Locate every blood parasite and identify its species.
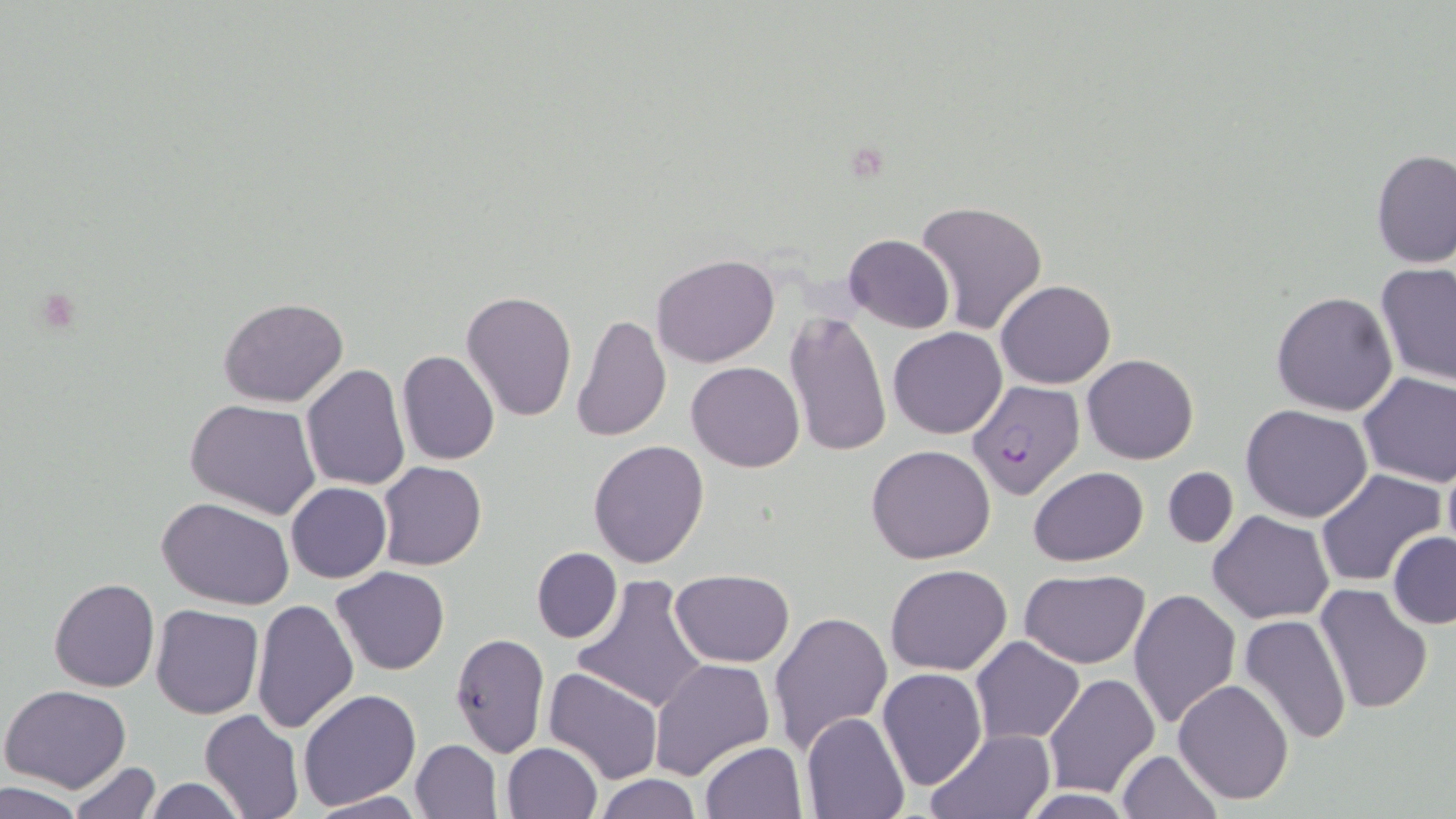
Approximate bounding boxes as (x1, y1, x2, y2) in pixels.
Plasmodium falciparum-infected red blood cells: (968, 380, 1085, 499).
No Plasmodium ovale, Plasmodium malariae, Plasmodium vivax, Babesia divergens, or Trypanosoma brucei observed.

Uninfected red blood cell locations: (1371, 149, 1456, 267), (915, 199, 1049, 337), (843, 234, 953, 334), (651, 253, 779, 368), (1373, 263, 1456, 386), (995, 280, 1116, 388), (461, 290, 578, 424), (1270, 290, 1399, 416), (218, 296, 349, 407), (783, 310, 892, 457), (577, 313, 683, 567), (571, 314, 672, 443), (888, 328, 1006, 439), (397, 350, 498, 465), (1082, 354, 1198, 464), (687, 360, 806, 472), (301, 363, 411, 490), (1358, 371, 1456, 488), (185, 399, 321, 520), (1240, 404, 1372, 522), (588, 440, 710, 568), (866, 444, 996, 565), (1439, 449, 1456, 564), (377, 461, 486, 570), (1162, 466, 1238, 548), (1028, 467, 1149, 564), (1316, 468, 1444, 589), (286, 482, 392, 583), (158, 496, 296, 607), (1207, 512, 1334, 625), (1388, 532, 1456, 629), (531, 547, 622, 644), (332, 565, 451, 675), (885, 565, 1012, 676), (670, 569, 795, 667), (1020, 569, 1151, 669), (49, 578, 160, 692), (572, 578, 711, 714), (1314, 585, 1434, 716), (1129, 587, 1241, 730), (250, 599, 358, 734), (151, 604, 263, 719), (768, 610, 893, 754), (1238, 613, 1353, 744), (449, 633, 550, 757), (971, 636, 1085, 744), (649, 658, 774, 780), (543, 667, 665, 785), (877, 667, 988, 790), (1044, 671, 1161, 795), (1173, 678, 1295, 804), (1, 684, 130, 793), (297, 689, 420, 812), (199, 710, 304, 819), (802, 713, 909, 818), (926, 727, 1056, 818), (410, 738, 503, 818), (700, 741, 808, 818), (501, 742, 602, 819), (1117, 750, 1222, 819), (67, 759, 162, 818), (593, 775, 704, 818), (141, 777, 250, 818), (1, 780, 88, 818), (1017, 788, 1139, 818), (305, 792, 424, 818). Slide-level diagnosis: Plasmodium falciparum. May-Grünwald-Giemsa stain. Thin blood smear. Optical microscopy. Single field of view. Image is 1456×819 pixels. Captured at 1000x magnification.